Identify the parasite.
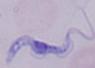

This is a trypanosome.

1000x magnification. Photomicrograph.